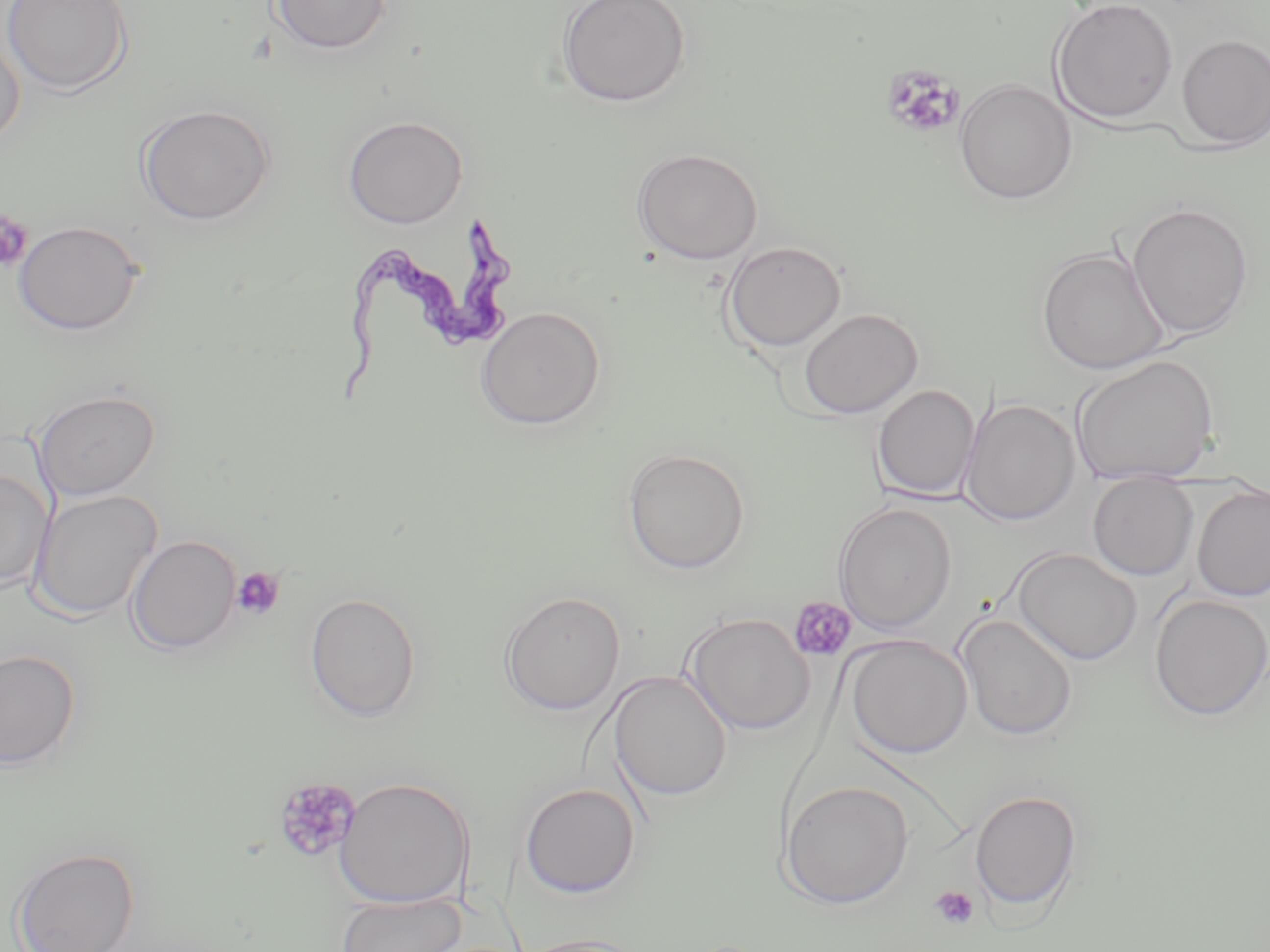

Summary:
  - Coordinate format: approximate bounding boxes as [x1, y1, x2, y2] in pixels
  - Trypanosoma brucei locations: [335, 218, 511, 402]
  - Uninfected red blood cell locations: [1, 0, 134, 96], [270, 0, 393, 55], [556, 0, 691, 108], [1050, 0, 1179, 124], [0, 27, 26, 150], [1177, 34, 1270, 150], [953, 77, 1077, 205], [136, 103, 275, 226], [342, 115, 469, 228], [631, 147, 764, 264], [1126, 202, 1254, 340], [12, 219, 145, 336], [723, 241, 846, 352], [1037, 246, 1169, 375], [474, 306, 606, 431], [798, 307, 922, 419], [1071, 355, 1220, 486], [872, 385, 979, 500], [33, 388, 161, 501], [962, 398, 1080, 526], [621, 446, 751, 574], [0, 468, 54, 590], [1088, 474, 1199, 580], [1191, 483, 1270, 602], [28, 489, 163, 620], [833, 502, 957, 634], [126, 535, 242, 654], [1011, 547, 1143, 666], [304, 591, 422, 723], [499, 591, 626, 716], [1149, 594, 1270, 720], [683, 612, 816, 735], [956, 614, 1078, 741], [845, 634, 972, 758], [0, 648, 82, 770], [608, 670, 732, 802], [334, 776, 474, 908], [778, 780, 914, 909], [519, 782, 641, 899], [969, 789, 1082, 912], [9, 845, 140, 951], [335, 892, 466, 952], [512, 934, 651, 952]
  - Platelet locations: [882, 66, 964, 140], [0, 211, 33, 271], [231, 567, 285, 620], [788, 596, 857, 662], [274, 777, 361, 864], [929, 885, 979, 931]
  - Slide-level diagnosis: Trypanosoma brucei
  - Modality: light microscopy
  - Image size: 1270×952 pixels
  - Stain: May-Grünwald-Giemsa
  - Field of view: single
  - Preparation: thin blood smear
  - Magnification: 1000x